Assess this cell for malaria.
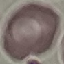

It is uninfected.

Summary:
  - Image type: automatically extracted cell patch, resized to 64 × 64 pixels
  - Stain: Giemsa
  - Capture: smartphone camera at the microscope eyepiece
  - Preparation: thin blood smear